Report the malaria status of this cell.
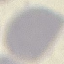
Uninfected.

Summary:
  - Preparation: thin blood smear
  - Image type: cell patch, automatically extracted from a larger field of view and resized to 64 × 64 pixels
  - Stain: Giemsa
  - Capture: smartphone through the microscope eyepiece